Classify this cell by malaria status.
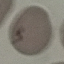
Uninfected.

Thin blood film. Acquired by smartphone through the microscope eyepiece. Giemsa-stained preparation. Cell patch, automatically extracted from a larger field of view and resized to 64 × 64 pixels.